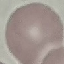
Summary:
  - Result: no malaria parasites detected
  - Image type: automatically extracted cell patch, resized to 64 × 64 pixels
  - Stain: Giemsa
  - Preparation: thin blood film
  - Capture: smartphone camera at the microscope eyepiece